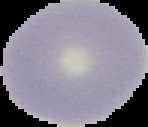

Summary:
  - Result: no malaria parasites seen
  - Preparation: thin blood film
  - Image type: segmented cell region with the area outside set to black
  - Image size: 148×127 pixels